Mark where platelets are.
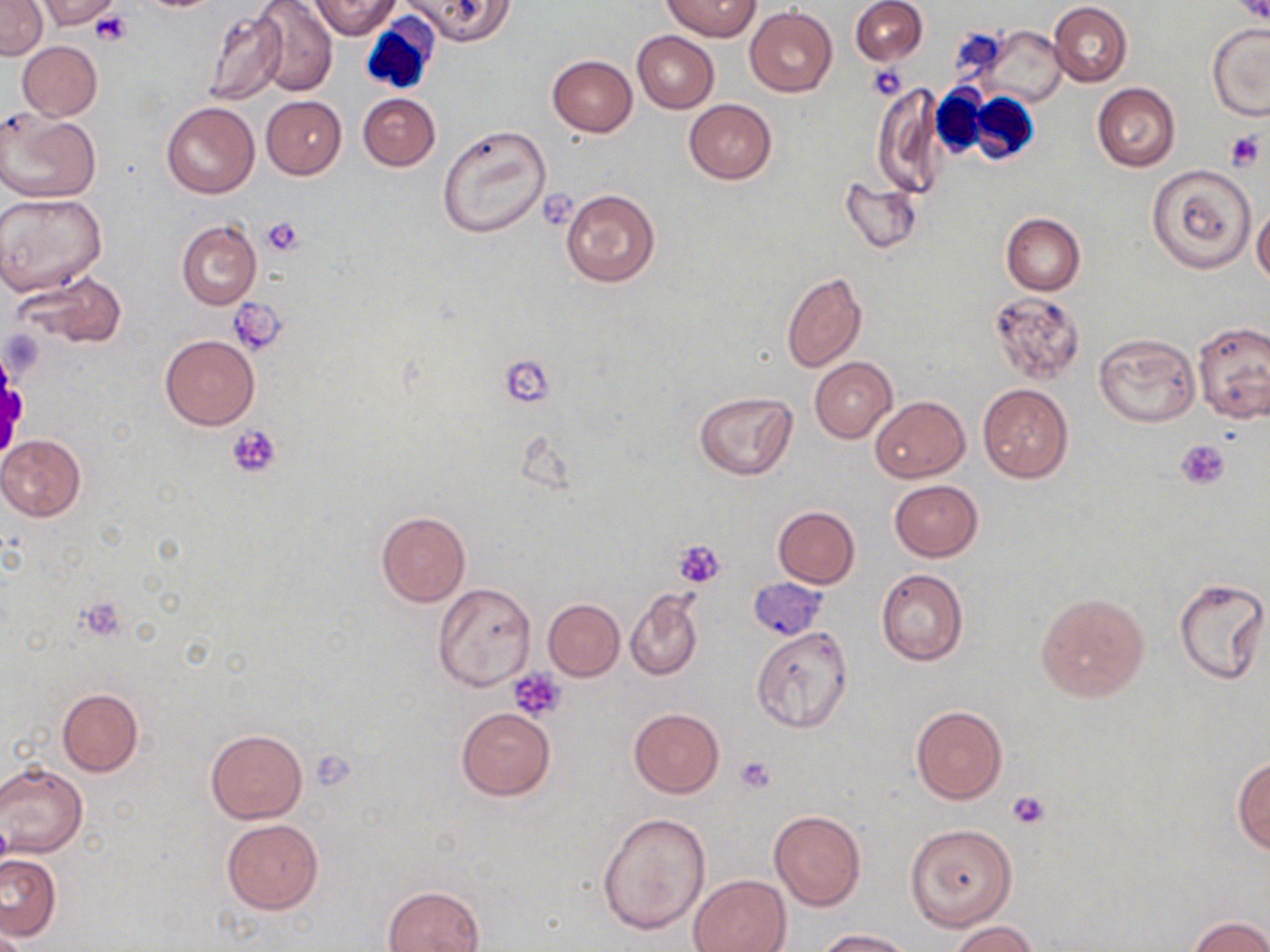

Approximate bounding boxes as named x1/y1/x2/y2 corners in pixels.
Platelets: (x1=88, y1=11, x2=133, y2=47), (x1=868, y1=64, x2=908, y2=99), (x1=1224, y1=130, x2=1265, y2=173), (x1=262, y1=215, x2=305, y2=258), (x1=228, y1=298, x2=287, y2=355), (x1=507, y1=356, x2=554, y2=410), (x1=227, y1=424, x2=281, y2=477), (x1=1177, y1=441, x2=1229, y2=490), (x1=674, y1=538, x2=726, y2=589), (x1=77, y1=597, x2=125, y2=641), (x1=509, y1=668, x2=566, y2=722), (x1=309, y1=752, x2=357, y2=790), (x1=734, y1=756, x2=777, y2=794), (x1=1007, y1=789, x2=1050, y2=829).

Uninfected red blood cell locations: (x1=0, y1=0, x2=47, y2=60), (x1=37, y1=0, x2=121, y2=30), (x1=251, y1=0, x2=337, y2=96), (x1=309, y1=0, x2=399, y2=38), (x1=405, y1=0, x2=515, y2=45), (x1=662, y1=0, x2=762, y2=41), (x1=850, y1=0, x2=927, y2=64), (x1=1049, y1=3, x2=1132, y2=86), (x1=203, y1=7, x2=288, y2=105), (x1=745, y1=7, x2=837, y2=97), (x1=975, y1=25, x2=1067, y2=106), (x1=1207, y1=25, x2=1270, y2=120), (x1=632, y1=30, x2=719, y2=113), (x1=17, y1=41, x2=102, y2=120), (x1=548, y1=55, x2=637, y2=136), (x1=871, y1=83, x2=946, y2=197), (x1=1092, y1=83, x2=1180, y2=171), (x1=358, y1=93, x2=440, y2=170), (x1=261, y1=96, x2=347, y2=179), (x1=684, y1=99, x2=776, y2=183), (x1=161, y1=103, x2=259, y2=199), (x1=1, y1=110, x2=100, y2=203), (x1=438, y1=123, x2=552, y2=239), (x1=1146, y1=166, x2=1254, y2=273), (x1=840, y1=178, x2=921, y2=253), (x1=560, y1=189, x2=661, y2=286), (x1=0, y1=192, x2=107, y2=296), (x1=1251, y1=208, x2=1270, y2=286), (x1=1001, y1=213, x2=1085, y2=295), (x1=177, y1=220, x2=261, y2=310), (x1=781, y1=270, x2=867, y2=372), (x1=19, y1=274, x2=125, y2=349), (x1=990, y1=290, x2=1085, y2=382), (x1=1192, y1=321, x2=1270, y2=423), (x1=1094, y1=332, x2=1200, y2=426), (x1=160, y1=335, x2=260, y2=429), (x1=811, y1=357, x2=897, y2=443), (x1=977, y1=384, x2=1073, y2=482), (x1=693, y1=392, x2=797, y2=480), (x1=870, y1=396, x2=969, y2=483), (x1=0, y1=434, x2=87, y2=522), (x1=889, y1=479, x2=984, y2=561), (x1=772, y1=506, x2=860, y2=588), (x1=375, y1=511, x2=471, y2=606), (x1=875, y1=568, x2=968, y2=665), (x1=1173, y1=578, x2=1268, y2=684), (x1=748, y1=579, x2=826, y2=640), (x1=433, y1=583, x2=536, y2=690), (x1=1036, y1=590, x2=1149, y2=702), (x1=626, y1=592, x2=703, y2=681), (x1=543, y1=599, x2=623, y2=680), (x1=750, y1=626, x2=854, y2=731), (x1=27, y1=688, x2=125, y2=818), (x1=57, y1=688, x2=143, y2=777), (x1=910, y1=706, x2=1007, y2=804), (x1=455, y1=707, x2=555, y2=800), (x1=629, y1=707, x2=724, y2=797), (x1=205, y1=729, x2=306, y2=823), (x1=1232, y1=756, x2=1270, y2=853), (x1=0, y1=761, x2=88, y2=858), (x1=769, y1=810, x2=866, y2=911), (x1=597, y1=811, x2=711, y2=934), (x1=221, y1=819, x2=324, y2=915), (x1=906, y1=823, x2=1017, y2=931), (x1=1, y1=854, x2=61, y2=941), (x1=688, y1=874, x2=791, y2=952), (x1=384, y1=885, x2=484, y2=952), (x1=1187, y1=916, x2=1270, y2=952), (x1=949, y1=921, x2=1040, y2=952), (x1=1, y1=928, x2=33, y2=952), (x1=816, y1=929, x2=915, y2=952). White blood cell locations: (x1=365, y1=13, x2=444, y2=92), (x1=935, y1=81, x2=988, y2=159), (x1=964, y1=91, x2=1039, y2=163). Slide-level diagnosis: no evidence of blood parasites. May-Grünwald-Giemsa-stained preparation. Optical microscopy. Image is 1270×952 pixels. Single field of view. Thin blood film. 1000x magnification.